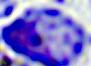
magnification = 400x
identification = leukocyte
modality = photomicrograph